Assess the morphology of the erythrocytes.
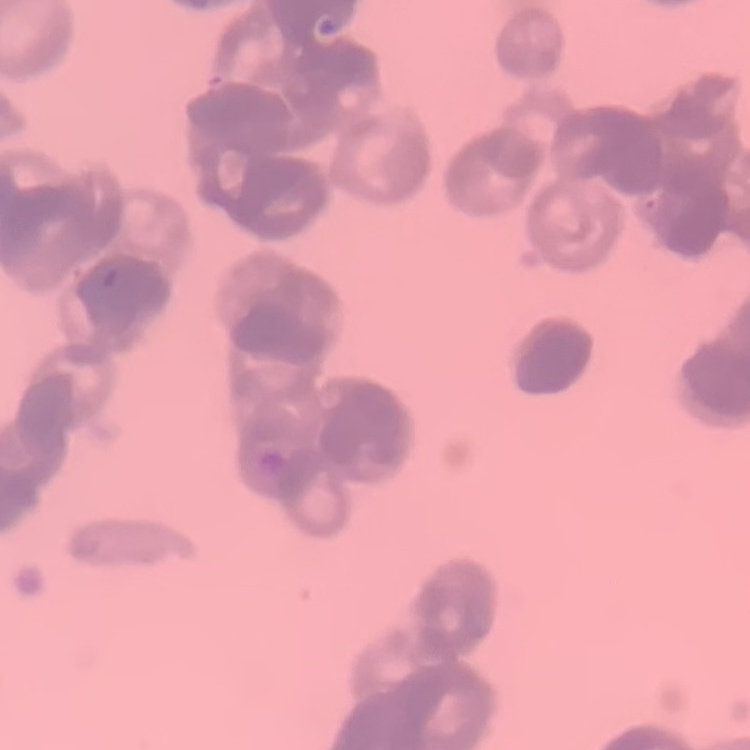

Rouleaux formation.

Summary:
  - Stain: Field's or Giemsa
  - Preparation: thin peripheral smear
  - Image type: one tile cut from a larger photomicrograph